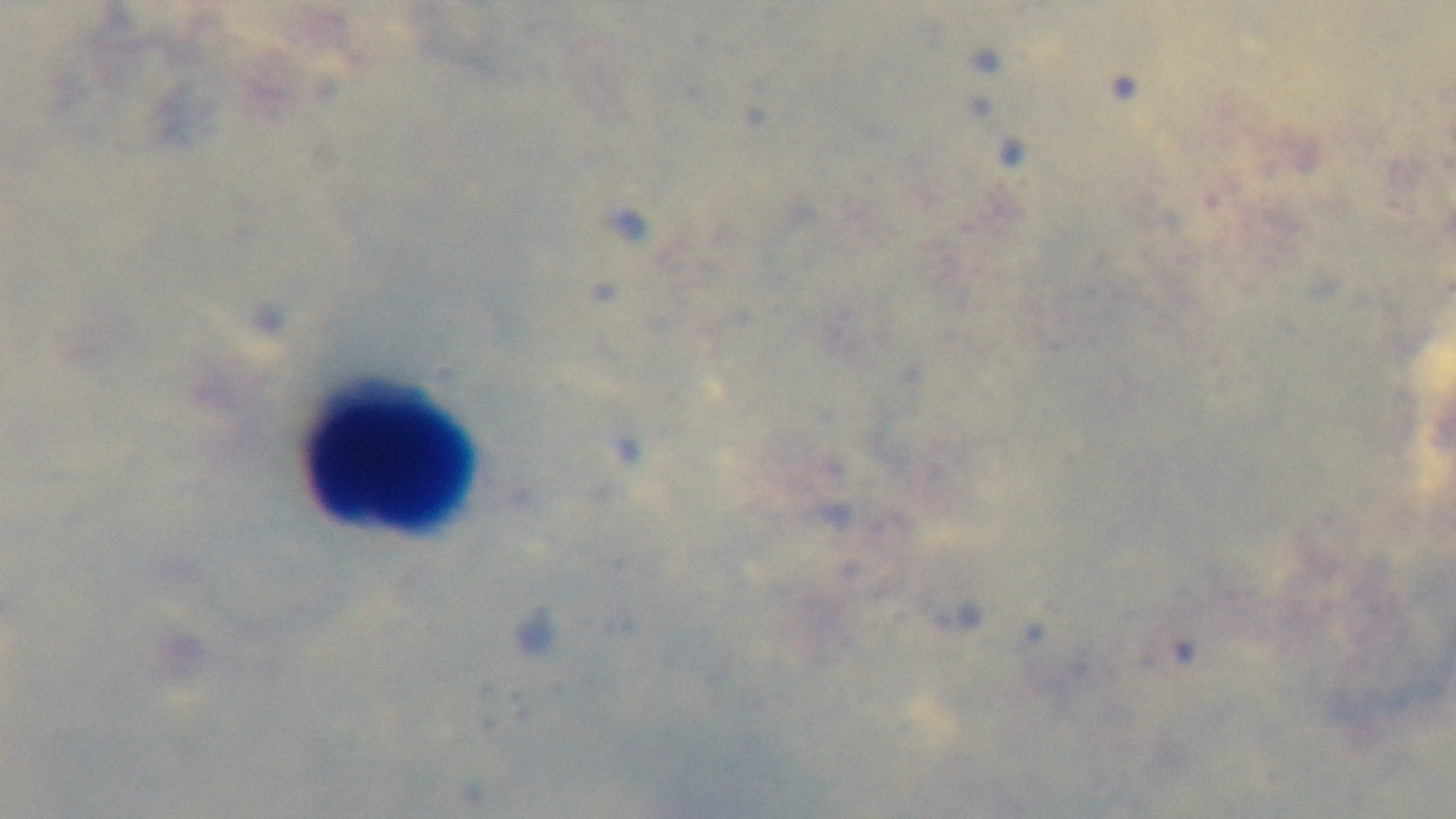
Summary:
  - Capture: mounted 4K digital camera
  - Field of view: one from the slide
  - Modality: light microscopy
  - Preparation: thick smear
  - Objective: 100x oil immersion
  - Stain: Giemsa
  - Malaria status: negative